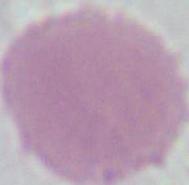 An erythrocyte is shown. Captured at 1000x magnification. Micrograph.